Report the malaria status of this cell.
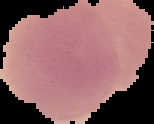

Uninfected.

image type = segmented cell region on a black background
image size = 154×124 pixels
preparation = thin blood smear